Outline each uninfected red blood cell.
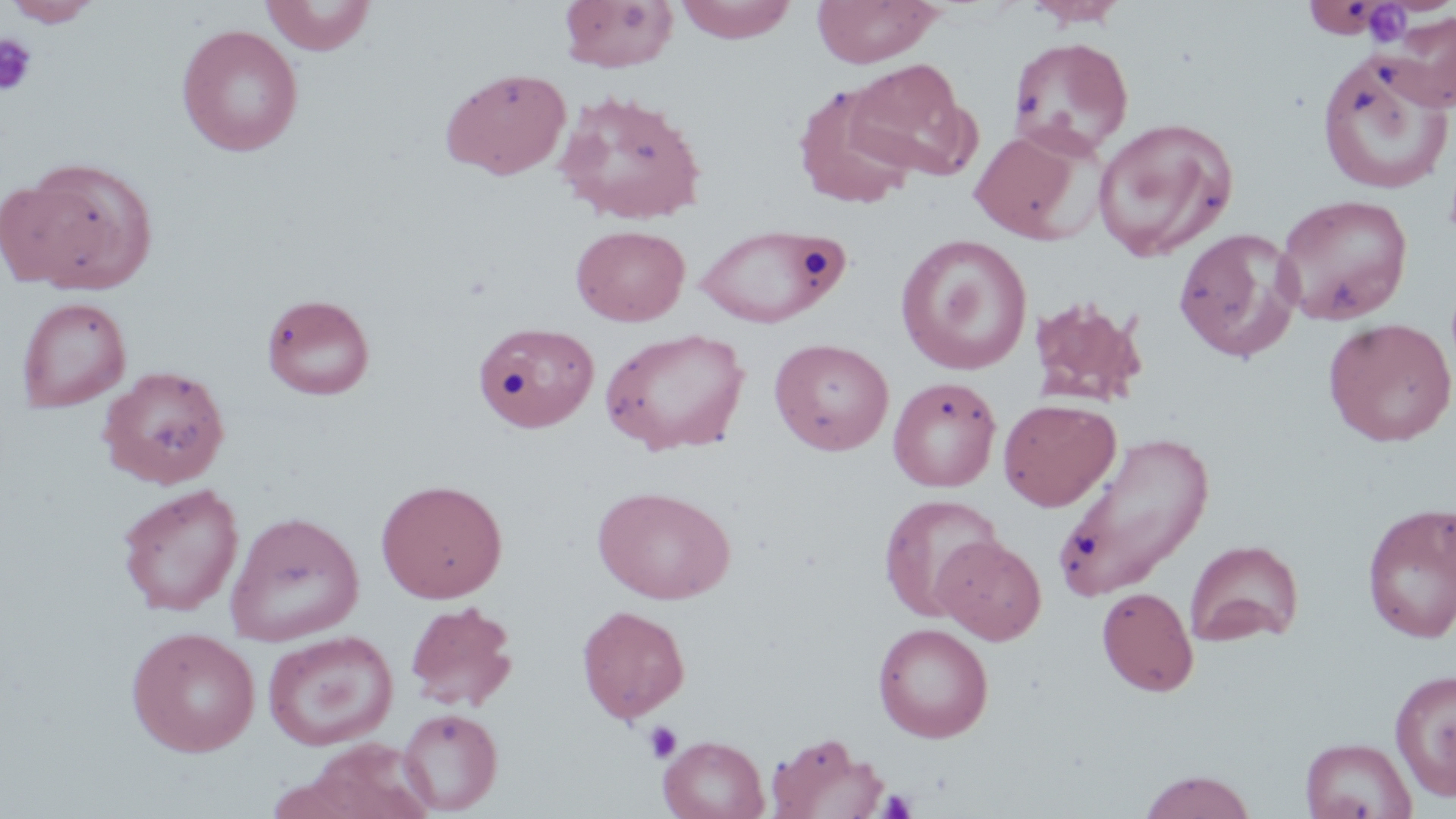

Approximate bounding boxes as [x1, y1, x2, y2] in pixels.
Uninfected red blood cells: [5, 0, 101, 27], [260, 0, 377, 55], [559, 0, 679, 72], [674, 0, 798, 43], [812, 0, 941, 67], [1024, 0, 1129, 30], [1302, 0, 1392, 39], [1382, 11, 1456, 111], [176, 24, 303, 156], [1008, 36, 1134, 159], [1315, 49, 1455, 196], [846, 56, 975, 181], [440, 67, 572, 180], [792, 83, 919, 210], [555, 89, 708, 225], [1093, 117, 1238, 262], [969, 127, 1091, 243], [8, 157, 157, 293], [1274, 193, 1414, 326], [694, 223, 846, 328], [571, 224, 690, 326], [1173, 228, 1303, 362], [896, 234, 1033, 375], [261, 293, 376, 400], [1027, 295, 1149, 408], [16, 296, 131, 411], [1323, 318, 1456, 447], [473, 321, 599, 433], [600, 327, 750, 454], [769, 337, 894, 456], [98, 364, 231, 490], [888, 376, 1001, 492], [998, 398, 1120, 511], [1052, 430, 1215, 604], [375, 479, 508, 603], [116, 483, 244, 616], [592, 485, 735, 604], [878, 494, 1003, 621], [1361, 502, 1456, 644], [225, 511, 364, 645], [932, 534, 1046, 645], [1186, 539, 1304, 647], [1097, 587, 1199, 697], [404, 600, 518, 711], [576, 605, 691, 724], [872, 622, 994, 742], [126, 626, 260, 757], [262, 630, 399, 751], [1389, 667, 1456, 801], [398, 708, 503, 814], [765, 732, 889, 819], [659, 735, 769, 819], [1300, 736, 1417, 819], [296, 739, 439, 819], [1138, 770, 1258, 818].

{
  "slide_level_diagnosis": "no evidence of blood parasites",
  "modality": "light microscopy",
  "image_size": "1456×819 pixels",
  "field_of_view": "single",
  "magnification": "1000x",
  "platelet_locations": "approximate bounding boxes as [x1, y1, x2, y2] in pixels: [1359, 3, 1413, 47], [0, 34, 39, 96], [1012, 91, 1045, 117], [644, 720, 682, 764], [878, 788, 917, 818]",
  "preparation": "thin blood smear",
  "stain": "May-Grünwald-Giemsa"
}